Report the malaria status.
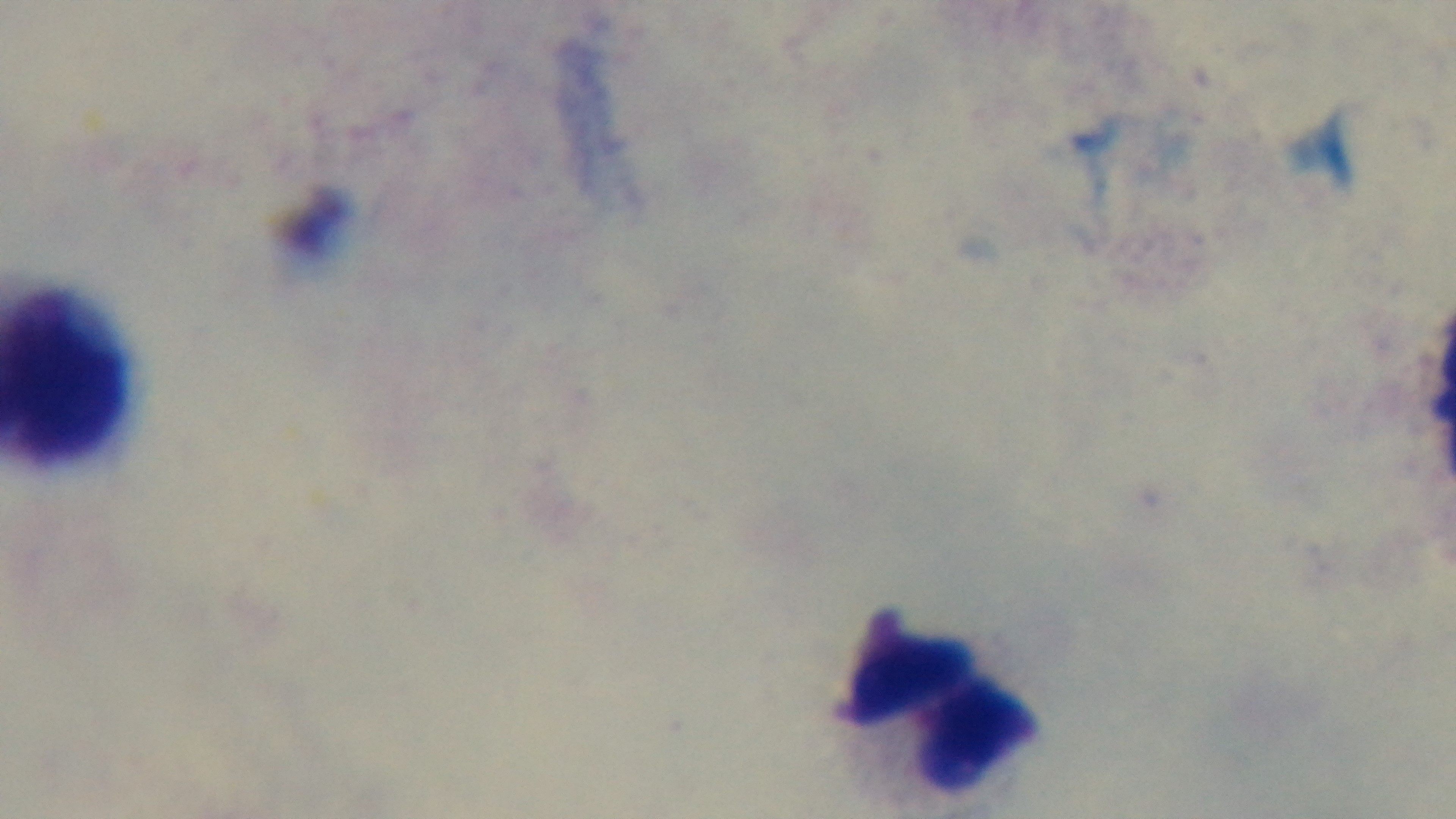
Negative.

Summary:
  - Objective: 100x oil immersion
  - Modality: light microscopy
  - Stain: Giemsa
  - Field of view: one from the slide
  - Preparation: thick
  - Capture: mounted 4K digital camera